Identify the parasite.
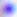

Toxoplasma gondii.

Summary:
  - Magnification: 400x
  - Modality: photomicrograph